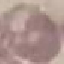
Summary:
  - Result: negative for malaria parasites
  - Capture: smartphone through the microscope eyepiece
  - Stain: Giemsa
  - Preparation: thin blood film
  - Image type: automatically extracted cell patch, resized to 64 × 64 pixels